Give the extent of all Plasmodium vivax-infected red blood cells.
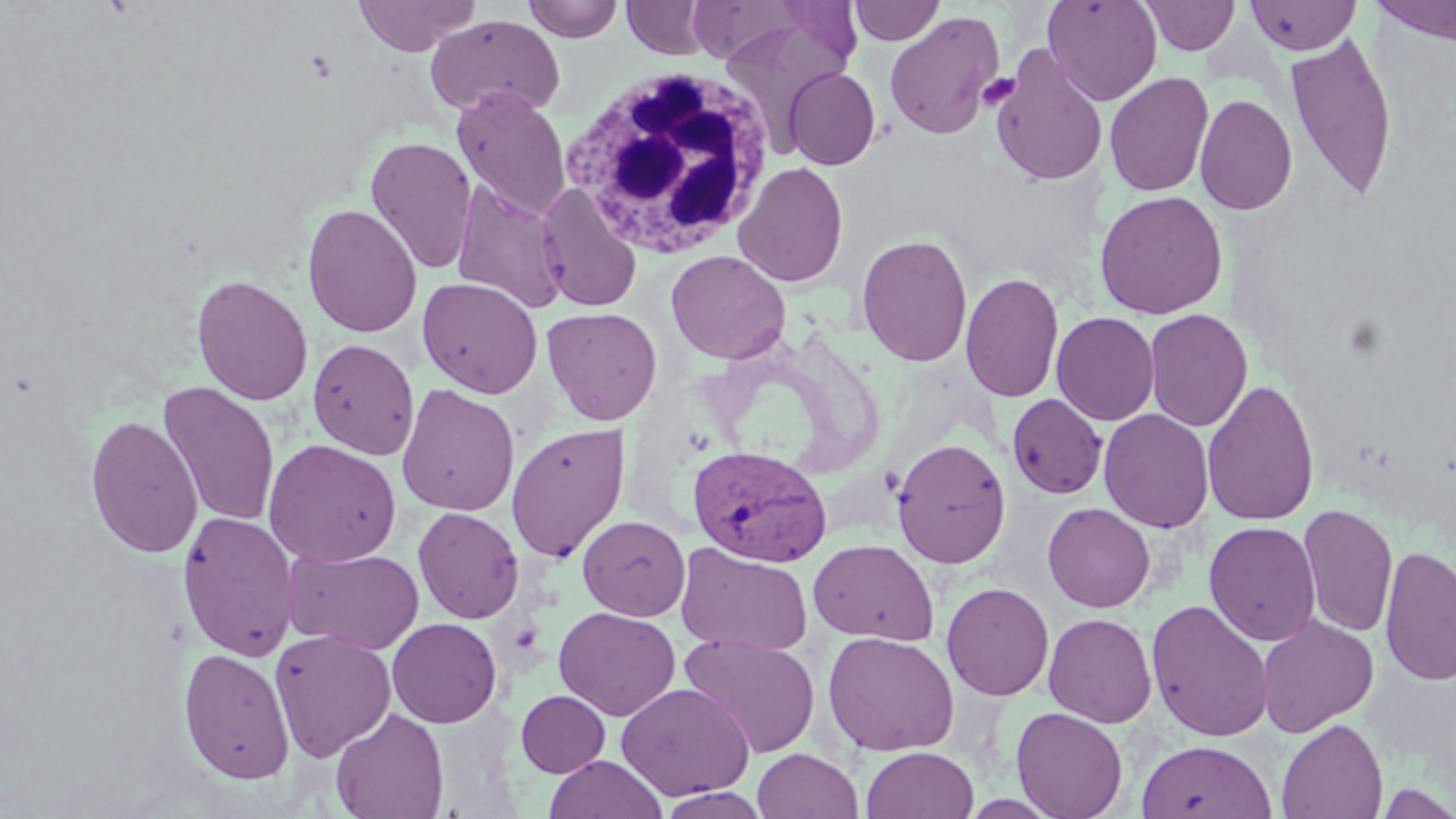

Approximate bounding boxes as [x1, y1, x2, y2] in pixels.
Plasmodium vivax-infected red blood cells: [687, 444, 832, 566].

slide_level_diagnosis: Plasmodium vivax
field_of_view: one of a larger specimen
magnification: 1000x
white_blood_cell_locations: 'approximate bounding boxes as [x1, y1, x2, y2] in pixels: [559, 66, 776, 257]'
uninfected_red_blood_cell_locations: 'approximate bounding boxes as [x1, y1, x2, y2] in pixels: [353, 0, 479, 55], [524, 0, 623, 42], [622, 0, 712, 59], [684, 0, 818, 65], [1043, 0, 1163, 105], [1139, 0, 1241, 55], [1245, 0, 1361, 55], [1370, 0, 1456, 44], [848, 1, 946, 45], [716, 8, 859, 142], [884, 11, 1005, 140], [425, 14, 566, 120], [1284, 33, 1398, 201], [990, 47, 1108, 187], [783, 67, 881, 170], [1105, 72, 1214, 197], [452, 86, 571, 221], [1195, 94, 1297, 215], [365, 136, 478, 275], [733, 161, 849, 287], [451, 179, 572, 313], [535, 183, 642, 312], [1094, 189, 1229, 319], [301, 202, 423, 338], [856, 231, 973, 367], [666, 250, 791, 365], [960, 271, 1064, 403], [191, 274, 313, 406], [417, 277, 543, 398], [542, 306, 663, 425], [1144, 308, 1253, 432], [1051, 311, 1160, 426], [308, 338, 419, 460], [1201, 378, 1320, 527], [158, 381, 280, 528], [396, 383, 520, 516], [1007, 393, 1107, 499], [1098, 408, 1214, 532], [85, 414, 202, 558], [506, 422, 630, 562], [891, 437, 1011, 569], [263, 439, 402, 567], [1043, 502, 1155, 612], [1298, 504, 1398, 638], [413, 506, 524, 624], [1324, 506, 1449, 655], [177, 510, 300, 662], [578, 514, 691, 621], [1204, 521, 1321, 647], [808, 539, 939, 644], [675, 543, 814, 656], [1379, 543, 1456, 687], [285, 546, 424, 655], [941, 582, 1054, 701], [1146, 598, 1275, 742], [554, 606, 681, 720], [1042, 612, 1157, 727], [1257, 615, 1379, 736], [386, 617, 502, 728], [270, 628, 396, 761], [823, 631, 959, 756], [678, 633, 821, 759], [178, 647, 295, 785], [617, 682, 755, 800], [516, 690, 611, 777], [1010, 706, 1129, 819], [330, 707, 449, 819], [1276, 718, 1389, 819], [1137, 740, 1276, 819], [861, 746, 979, 819], [752, 748, 863, 819], [544, 754, 667, 819], [1375, 781, 1456, 818]'
modality: light microscopy
stain: May-Grünwald-Giemsa
image_size: 1456×819 pixels
platelet_locations: 'approximate bounding boxes as [x1, y1, x2, y2] in pixels: [978, 74, 1019, 109]'
preparation: thin blood film